Locate every malaria parasite.
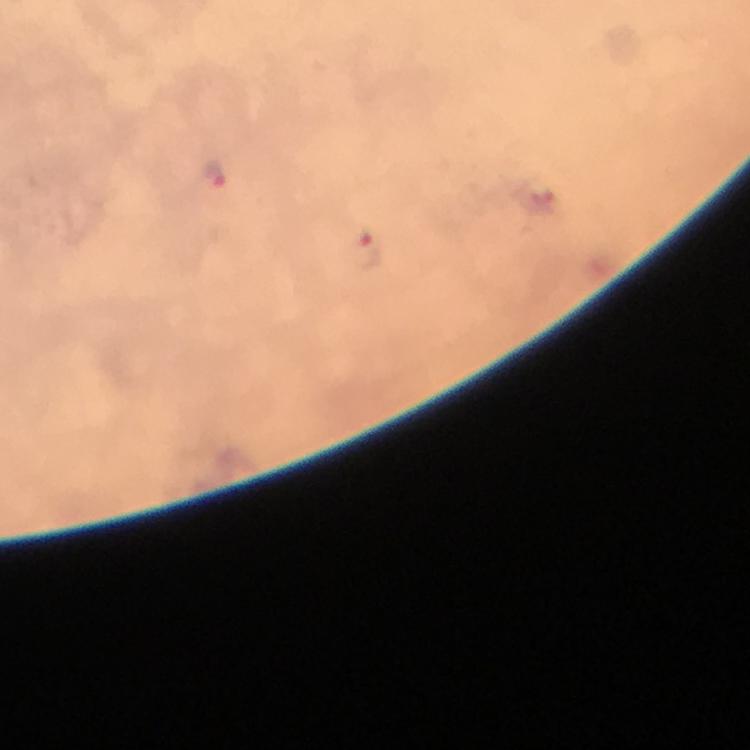

Approximate object centers, in pixels from the top-left corner.
Malaria parasites: (x=213, y=174), (x=367, y=253).

Thick blood film. From a diagnostic examination for malaria. At 100x magnification. Photographed through the microscope with a smartphone camera. Immersion oil applied. Giemsa-stained preparation. Cropped region of a single field of view. Image is 750×750 pixels.